Classify this cell by malaria status.
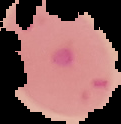

Parasitized.

Summary:
  - Image type: segmented cell region with the area outside set to black
  - Preparation: thin blood film
  - Image size: 121×124 pixels